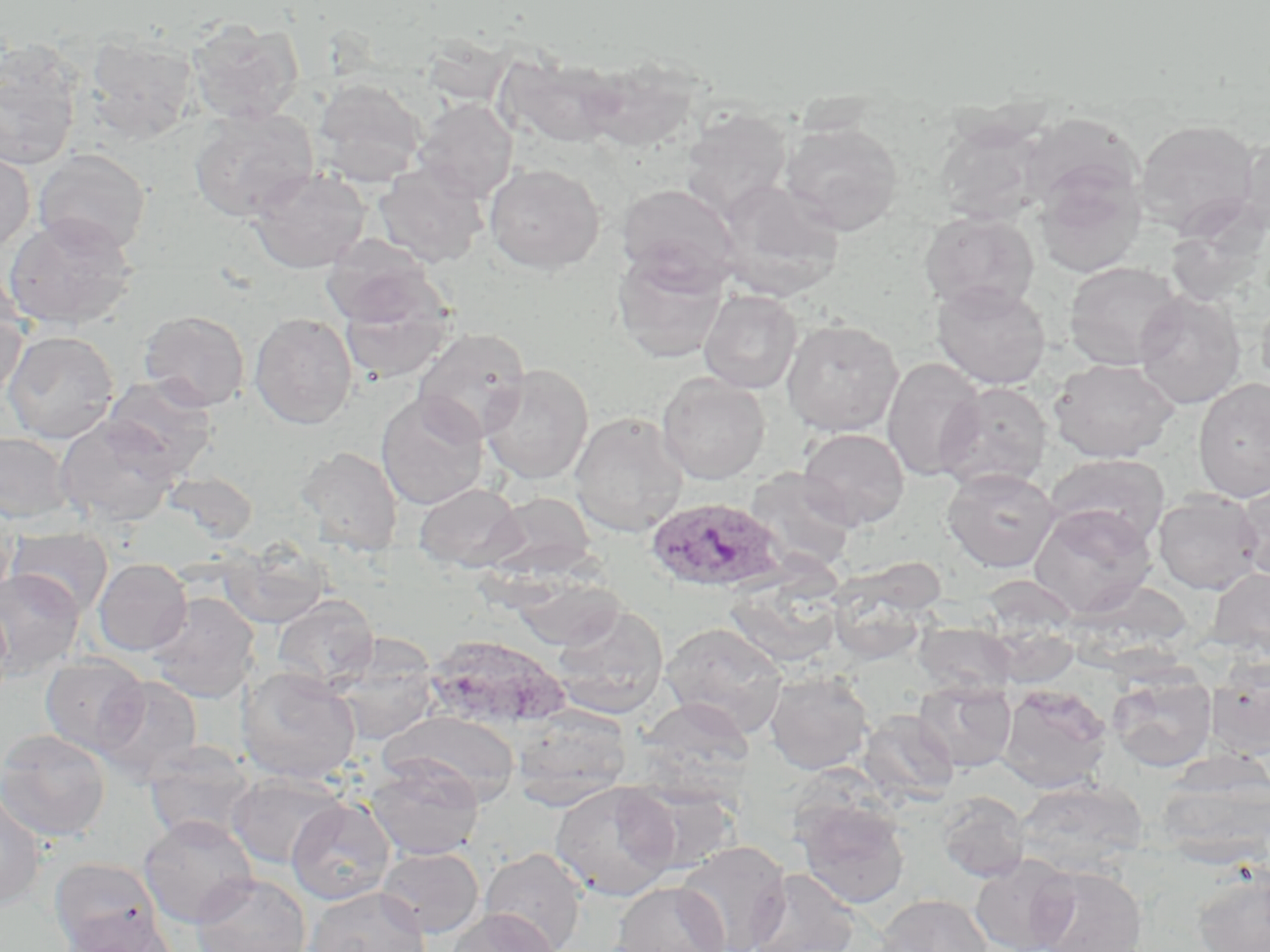
{
  "slide_level_diagnosis": "Plasmodium ovale",
  "field_of_view": "one of a larger specimen",
  "magnification": "1000x",
  "uninfected_red_blood_cell_locations": "approximate bounding boxes as (x1, y1, x2, y2) in pixels: (186, 19, 304, 124), (83, 32, 200, 143), (0, 41, 84, 171), (496, 54, 621, 149), (577, 56, 700, 153), (312, 77, 428, 187), (414, 99, 518, 203), (188, 107, 320, 222), (679, 107, 793, 222), (1022, 113, 1143, 214), (934, 118, 1051, 226), (1134, 118, 1262, 239), (780, 121, 904, 235), (1237, 131, 1270, 239), (0, 148, 35, 255), (33, 149, 151, 256), (373, 162, 489, 268), (484, 162, 605, 274), (1034, 162, 1146, 278), (248, 166, 371, 273), (714, 178, 844, 301), (616, 183, 741, 290), (919, 212, 1040, 313), (2, 215, 137, 330), (320, 237, 439, 327), (612, 251, 729, 363), (1064, 261, 1186, 371), (0, 271, 29, 399), (931, 280, 1051, 389), (339, 290, 455, 384), (699, 290, 802, 394), (1133, 290, 1246, 409), (1256, 293, 1270, 392), (138, 310, 250, 411), (249, 312, 357, 429), (781, 318, 903, 437), (412, 327, 531, 443), (2, 330, 120, 444), (881, 357, 987, 482), (1048, 357, 1181, 463), (480, 364, 594, 485), (657, 373, 770, 484), (102, 375, 218, 479), (1193, 378, 1270, 503), (936, 381, 1052, 491), (375, 392, 489, 510), (569, 411, 689, 538), (55, 416, 180, 528), (797, 427, 910, 531), (0, 432, 73, 524), (294, 446, 404, 557), (1045, 453, 1170, 551), (942, 466, 1059, 573), (745, 468, 858, 574), (163, 470, 258, 544), (1234, 479, 1270, 581), (413, 482, 526, 573), (1153, 491, 1264, 594), (483, 492, 598, 579), (0, 499, 18, 603), (1030, 504, 1157, 619), (6, 527, 114, 620), (219, 542, 333, 629), (93, 558, 192, 656), (1207, 568, 1270, 660), (0, 569, 85, 676), (826, 572, 934, 667), (511, 575, 624, 650), (724, 579, 843, 669), (145, 592, 259, 703), (272, 594, 378, 693), (0, 598, 13, 709), (551, 605, 669, 719), (987, 620, 1081, 687), (913, 621, 1016, 700), (661, 622, 788, 737), (424, 635, 569, 732), (330, 640, 440, 746), (40, 654, 149, 756), (1206, 657, 1270, 758), (236, 667, 361, 784), (1107, 669, 1216, 772), (764, 670, 873, 775), (95, 675, 203, 783), (914, 680, 1016, 772), (998, 685, 1112, 793), (637, 698, 754, 794), (511, 705, 632, 810), (857, 709, 959, 807), (381, 710, 521, 806), (0, 729, 111, 842), (143, 742, 258, 846), (366, 758, 484, 861), (1156, 758, 1270, 866), (227, 773, 346, 870), (1015, 778, 1147, 874), (549, 780, 682, 902), (628, 784, 742, 874), (0, 789, 47, 910), (937, 791, 1030, 883), (794, 796, 911, 909), (285, 798, 395, 905), (139, 815, 258, 928), (675, 841, 791, 952), (376, 846, 485, 938), (481, 847, 587, 952), (970, 855, 1077, 952), (49, 857, 160, 952), (1030, 865, 1147, 952), (1191, 866, 1270, 952), (746, 868, 861, 952), (192, 873, 311, 952), (611, 881, 730, 952), (304, 886, 430, 952), (875, 894, 994, 952), (447, 907, 560, 952), (65, 913, 177, 952)",
  "image_size": "1270×952 pixels",
  "stain": "May-Grünwald-Giemsa",
  "preparation": "thin blood smear",
  "plasmodium_ovale_infected_red_blood_cell_locations": "approximate bounding boxes as (x1, y1, x2, y2) in pixels: (646, 497, 789, 594)",
  "modality": "light microscopy"
}